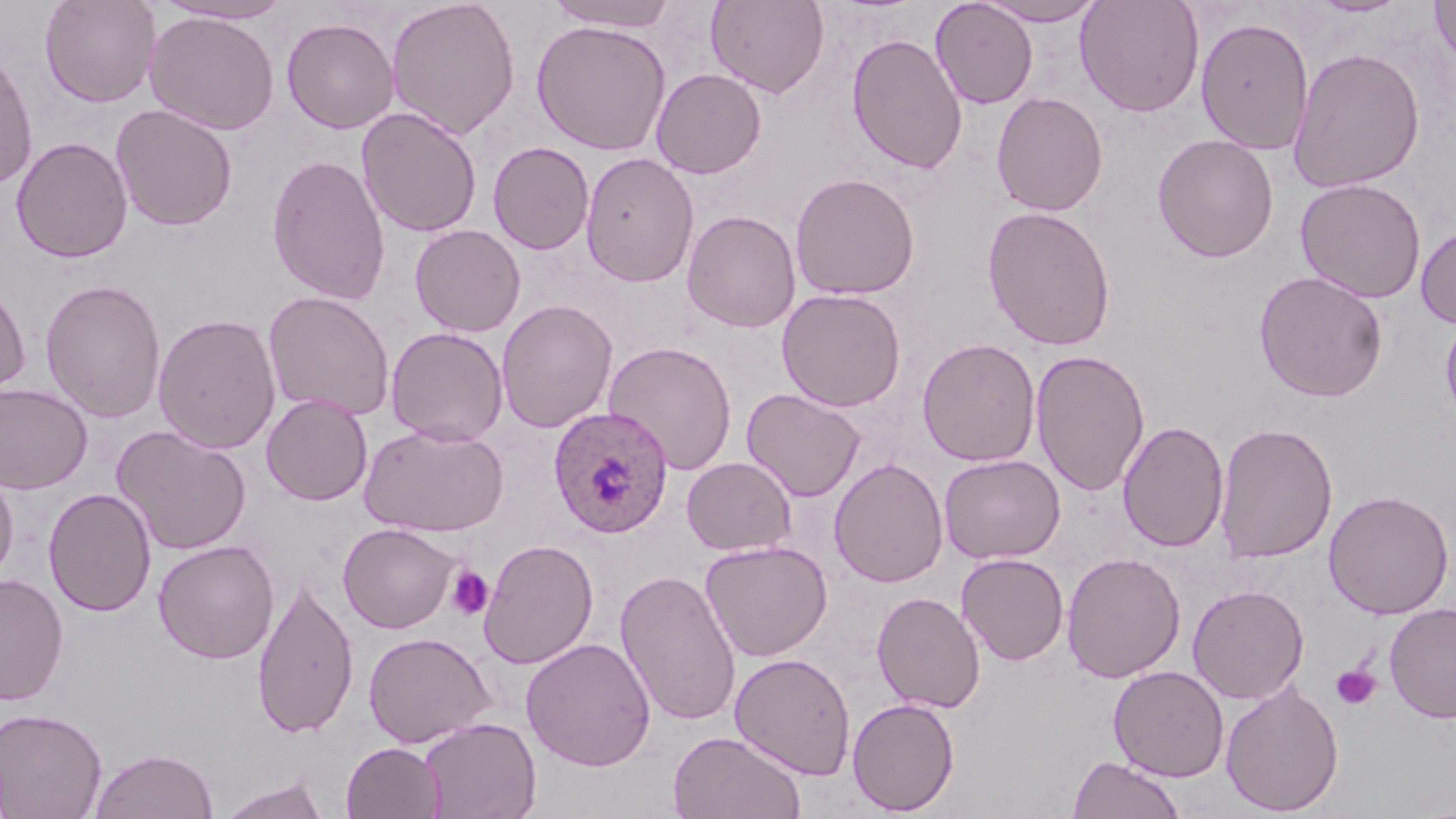

slide-level diagnosis = Plasmodium ovale
stain = May-Grünwald-Giemsa
field of view = single
image size = 1456×819 pixels
Plasmodium ovale-infected red blood cell locations = approximate bounding boxes as [x1, y1, x2, y2] in pixels: [549, 405, 673, 538]
platelet locations = approximate bounding boxes as [x1, y1, x2, y2] in pixels: [446, 564, 494, 621], [1331, 664, 1381, 712]
preparation = thin blood smear
uninfected red blood cell locations = approximate bounding boxes as [x1, y1, x2, y2] in pixels: [39, 0, 161, 108], [385, 0, 521, 139], [547, 0, 679, 31], [705, 0, 830, 98], [930, 0, 1039, 109], [976, 0, 1107, 25], [1075, 0, 1205, 117], [1308, 0, 1412, 17], [1430, 0, 1456, 70], [155, 1, 296, 25], [144, 10, 280, 135], [1195, 16, 1314, 155], [281, 17, 400, 134], [531, 20, 672, 156], [847, 32, 967, 174], [1288, 46, 1425, 193], [0, 49, 39, 189], [650, 68, 766, 178], [991, 92, 1108, 216], [111, 104, 238, 231], [356, 107, 482, 238], [1152, 133, 1279, 262], [11, 136, 133, 263], [488, 141, 595, 255], [266, 152, 391, 305], [580, 152, 700, 288], [789, 172, 921, 300], [1295, 178, 1427, 303], [1276, 180, 1409, 399], [982, 205, 1117, 350], [682, 209, 801, 333], [409, 224, 526, 337], [1416, 224, 1456, 328], [1254, 271, 1388, 402], [40, 279, 167, 423], [0, 280, 32, 402], [776, 288, 906, 411], [263, 291, 395, 421], [496, 299, 617, 433], [1440, 310, 1456, 431], [152, 312, 282, 454], [386, 326, 509, 445], [917, 337, 1041, 467], [603, 340, 738, 475], [1030, 348, 1150, 498], [0, 383, 93, 494], [742, 387, 866, 502], [261, 393, 373, 506], [1118, 420, 1228, 553], [359, 422, 508, 537], [1215, 422, 1338, 564], [112, 425, 252, 556], [939, 454, 1065, 564], [682, 456, 797, 556], [829, 457, 949, 588], [0, 460, 19, 586], [43, 488, 157, 616], [1323, 489, 1454, 619], [339, 523, 458, 633], [153, 539, 279, 664], [479, 539, 599, 669], [699, 540, 833, 662], [1061, 551, 1186, 683], [956, 553, 1069, 665], [615, 568, 742, 727], [0, 573, 69, 706], [251, 576, 359, 740], [1187, 584, 1310, 704], [871, 591, 986, 713], [1384, 602, 1456, 724], [362, 631, 496, 748], [520, 637, 657, 771], [730, 652, 856, 780], [1107, 665, 1229, 782], [1220, 681, 1344, 816], [847, 697, 960, 815], [0, 706, 108, 818], [419, 717, 541, 819], [668, 730, 806, 819], [341, 742, 446, 819], [89, 747, 218, 819], [1068, 754, 1185, 818], [217, 775, 331, 819]
modality = optical microscopy
magnification = 1000x